Report the malaria status of this cell.
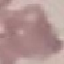

Uninfected.

Thin blood film. Giemsa stain. Photographed with a smartphone camera at the microscope eyepiece. Cell patch, automatically extracted from a larger field of view and resized to 64 × 64 pixels.